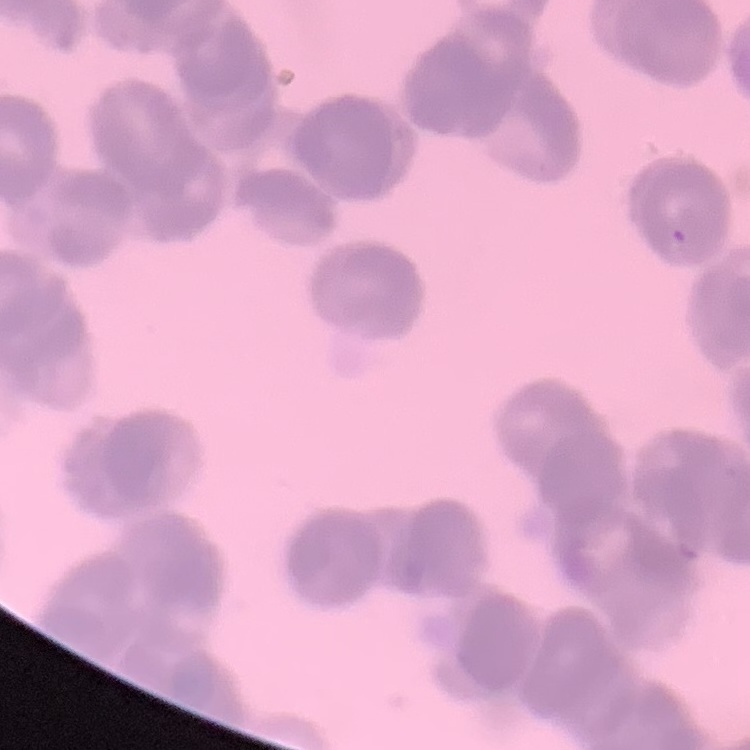

Summary:
  - Red blood cell morphology: rouleaux formation
  - Image type: square crop of a larger photomicrograph
  - Stain: Field's or Giemsa
  - Preparation: thin blood smear